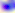
identification: Toxoplasma gondii
modality: photomicrograph
magnification: 400x